Comment on the morphology of the red blood cells.
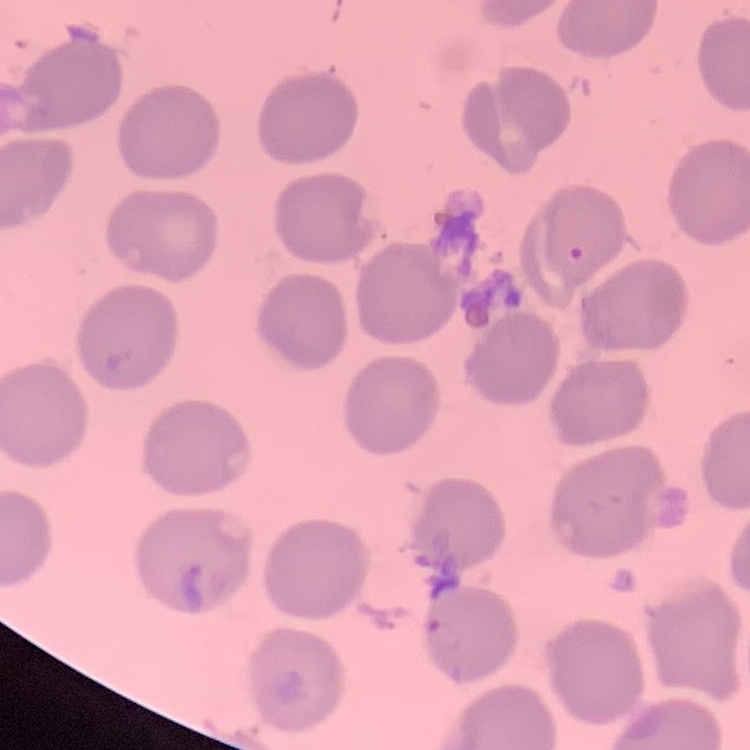

No rouleaux formation.

Stained with either Field's or Giemsa. One tile cut from a larger photomicrograph. Thin blood film.